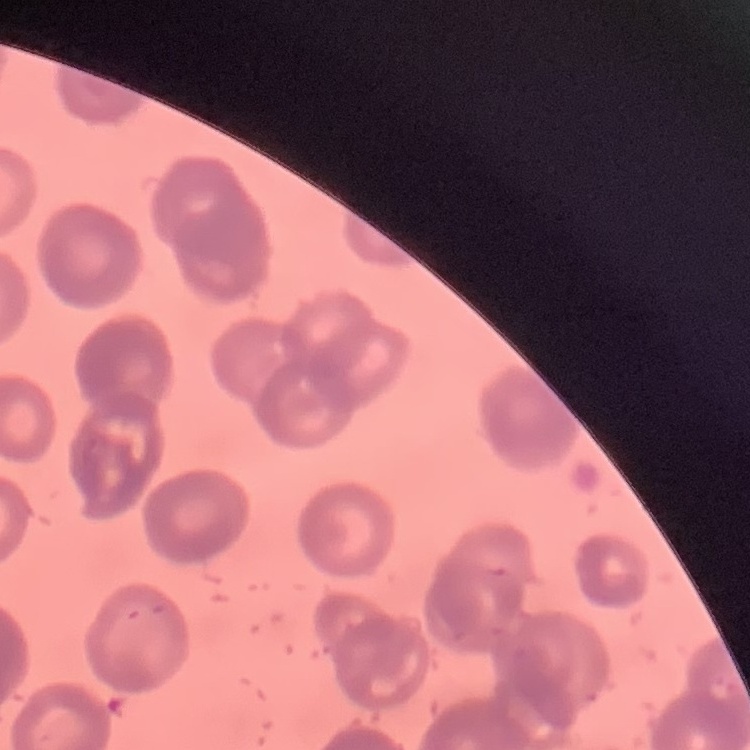

The red blood cells show rouleaux formation. Stained with either Field's or Giemsa. Square crop of a larger photomicrograph. Thin peripheral smear.